Outline each blood parasite and name the species.
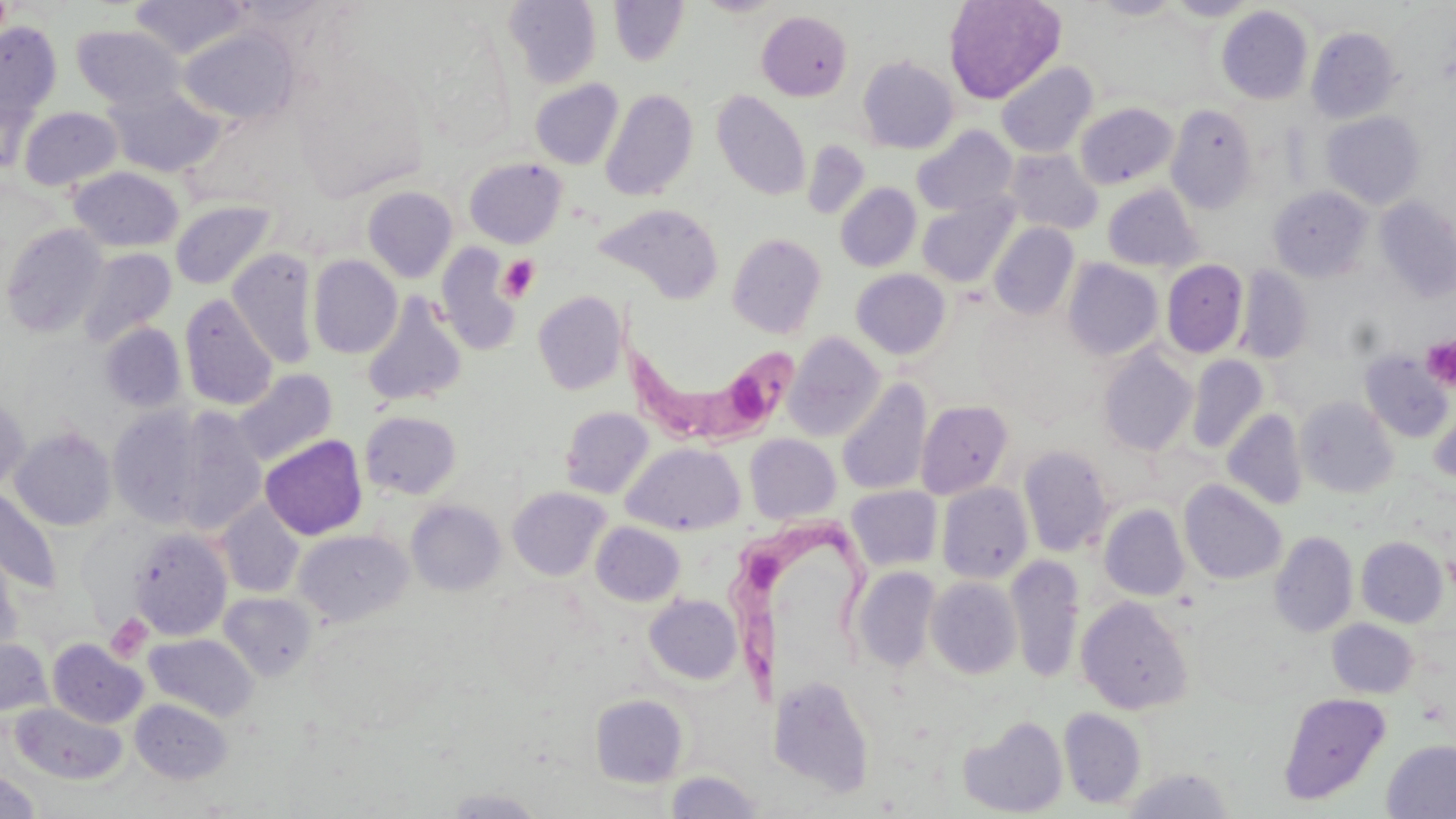
Approximate bounding boxes as [x1, y1, x2, y2] in pixels.
Trypanosoma brucei: [613, 333, 800, 444], [732, 514, 879, 704].
No Plasmodium falciparum, Plasmodium ovale, Plasmodium malariae, Plasmodium vivax, or Babesia divergens observed.

Summary:
  - Platelet locations: [498, 255, 540, 302], [1420, 335, 1456, 391], [106, 613, 152, 663]
  - Uninfected red blood cell locations: [129, 0, 251, 59], [609, 0, 688, 66], [697, 0, 784, 17], [943, 0, 1066, 104], [1092, 0, 1183, 20], [1166, 0, 1259, 21], [503, 1, 601, 88], [1216, 6, 1313, 104], [757, 10, 852, 101], [0, 21, 62, 123], [71, 24, 186, 110], [177, 24, 299, 126], [1306, 27, 1402, 123], [858, 56, 958, 153], [996, 61, 1098, 158], [530, 79, 623, 170], [102, 84, 225, 178], [600, 88, 698, 202], [711, 90, 811, 201], [1075, 102, 1178, 189], [1166, 104, 1257, 213], [18, 106, 123, 190], [1322, 111, 1425, 209], [912, 125, 1018, 216], [802, 140, 870, 220], [1004, 149, 1103, 234], [464, 157, 566, 248], [69, 166, 184, 252], [835, 183, 921, 272], [1102, 184, 1202, 272], [362, 186, 458, 283], [1268, 186, 1373, 282], [918, 197, 1018, 288], [1374, 197, 1456, 304], [170, 201, 277, 290], [594, 203, 724, 304], [989, 222, 1079, 320], [1, 223, 110, 338], [727, 233, 827, 338], [435, 243, 522, 357], [77, 247, 177, 347], [227, 248, 318, 369], [308, 255, 402, 359], [1063, 259, 1163, 360], [1161, 259, 1247, 358], [1236, 265, 1312, 364], [851, 269, 951, 359], [533, 290, 627, 395], [180, 294, 278, 410], [361, 294, 467, 408], [99, 322, 187, 413], [784, 333, 885, 441], [1098, 346, 1197, 456], [1359, 350, 1453, 443], [1187, 355, 1269, 455], [233, 369, 338, 467], [836, 378, 932, 496], [0, 394, 30, 493], [1296, 396, 1399, 498], [916, 400, 1013, 499], [1427, 402, 1456, 485], [108, 406, 208, 527], [166, 407, 267, 535], [560, 407, 653, 498], [1223, 409, 1307, 510], [359, 411, 461, 499], [9, 426, 118, 531], [745, 434, 841, 524], [260, 435, 368, 540], [621, 442, 745, 536], [1018, 445, 1114, 557], [1179, 480, 1286, 585], [937, 482, 1033, 584], [846, 485, 942, 571], [507, 486, 611, 581], [0, 487, 63, 594], [217, 500, 305, 598], [407, 500, 506, 595], [1099, 505, 1190, 601], [591, 522, 685, 606], [129, 527, 232, 640], [294, 529, 413, 626], [1270, 531, 1358, 638], [1356, 536, 1447, 627], [0, 542, 24, 660], [1007, 555, 1085, 684], [852, 566, 940, 671], [926, 577, 1021, 679], [219, 592, 318, 680], [645, 594, 742, 684], [1076, 596, 1194, 715], [1327, 619, 1418, 698], [144, 633, 258, 720], [0, 637, 52, 717], [48, 639, 147, 728], [768, 673, 876, 796], [1278, 692, 1391, 805], [590, 694, 689, 787], [130, 698, 233, 783], [11, 702, 127, 785], [1059, 708, 1146, 809], [958, 715, 1068, 817], [1382, 740, 1456, 819], [1121, 766, 1236, 818], [1, 769, 40, 818], [664, 770, 765, 818], [441, 788, 547, 818]
  - Slide-level diagnosis: Trypanosoma brucei
  - Image size: 1456×819 pixels
  - Field of view: one of a larger specimen
  - Preparation: thin blood film
  - Stain: May-Grünwald-Giemsa
  - Magnification: 1000x
  - Modality: light microscopy